Name the cell type shown.
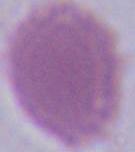

An erythrocyte.

magnification = 1000x
modality = photomicrograph